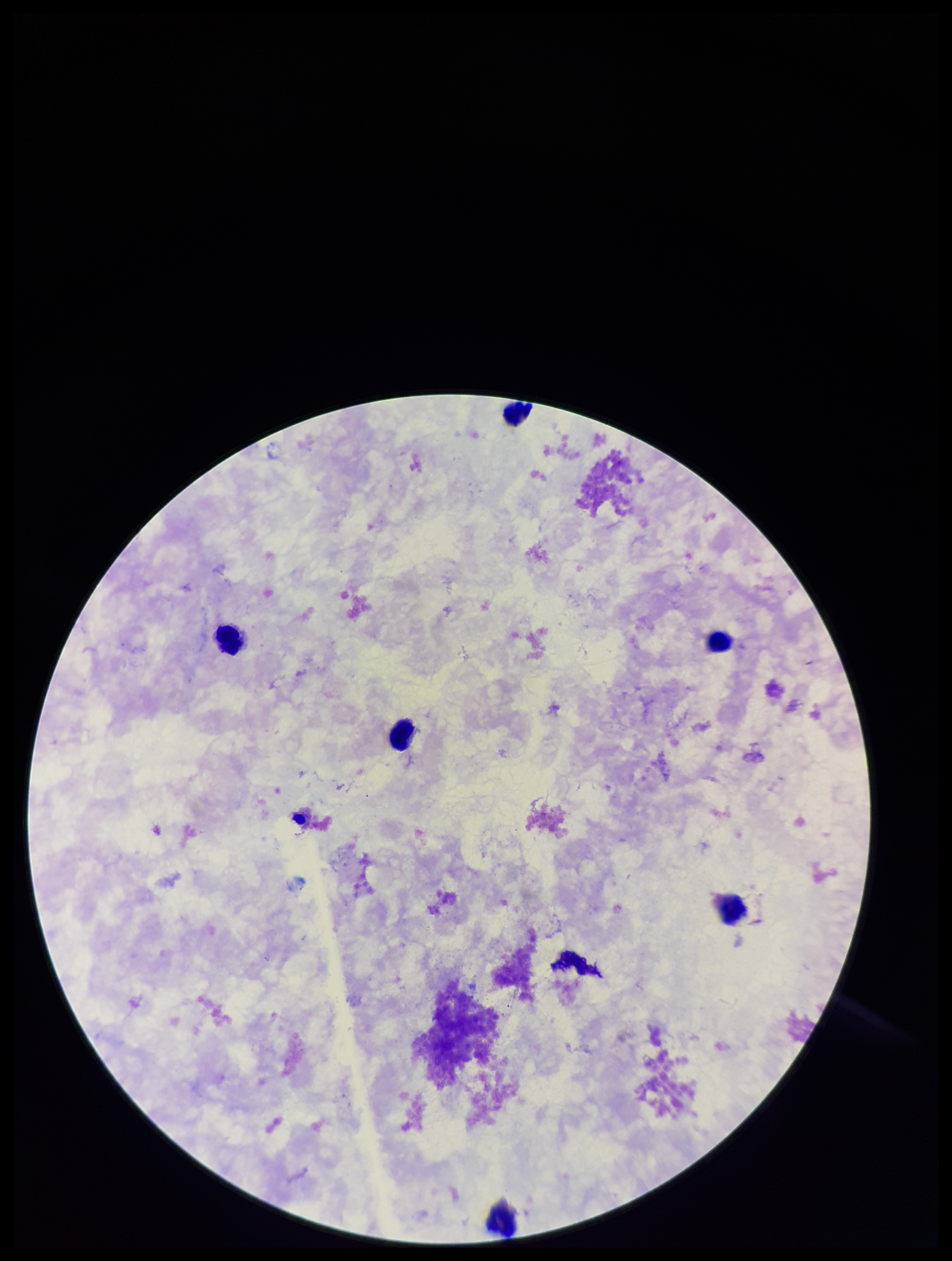

Summary:
  - Field of view: one from this slide
  - Leukocyte count: 6
  - Image size: 952×1261 pixels
  - Parasite count: 0
  - Plasmodium parasites: none identified
  - Preparation: thick blood smear
  - Patient malaria status: negative
  - Capture: smartphone photograph through the microscope eyepiece
  - Stain: Giemsa